Assess the morphology of the erythrocytes.
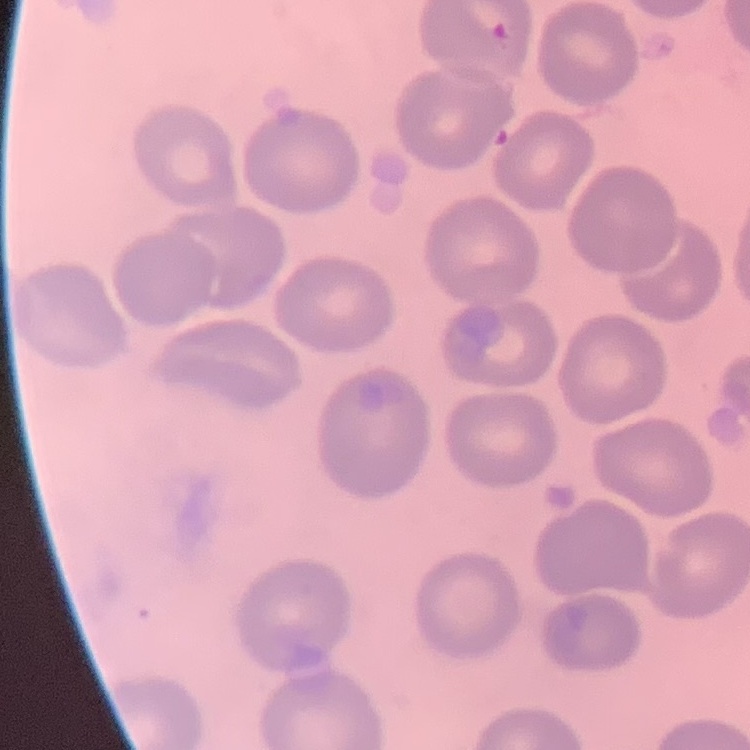
No rouleaux formation.

preparation = thin blood film
image type = one tile cut from a larger photomicrograph
stain = Field's or Giemsa